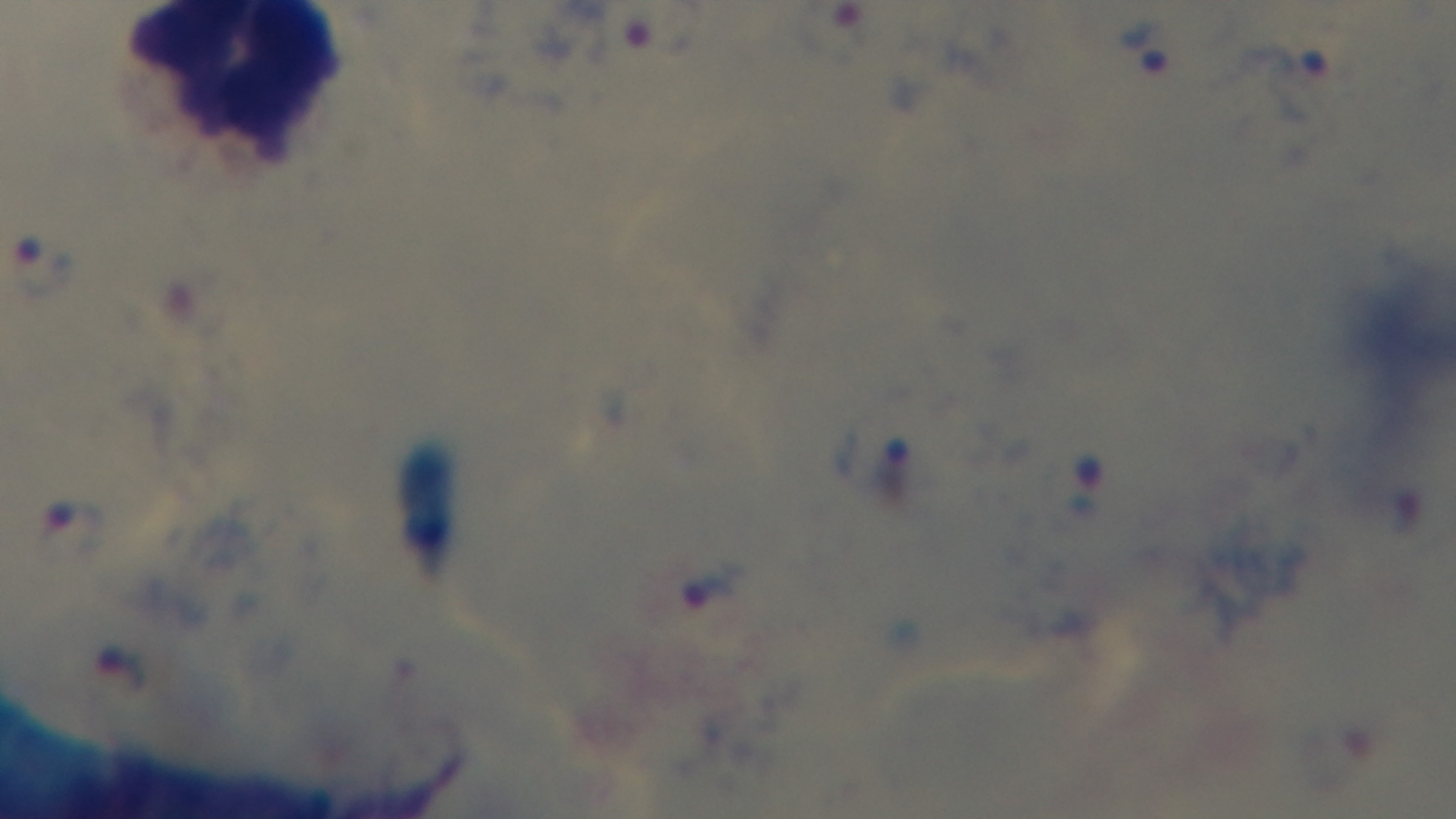
{
  "capture": "mounted 4K digital camera",
  "stain": "Giemsa",
  "modality": "light microscopy",
  "objective": "100x oil immersion",
  "malaria_status": "positive",
  "field_of_view": "single",
  "preparation": "thick smear"
}